Identify the parasite.
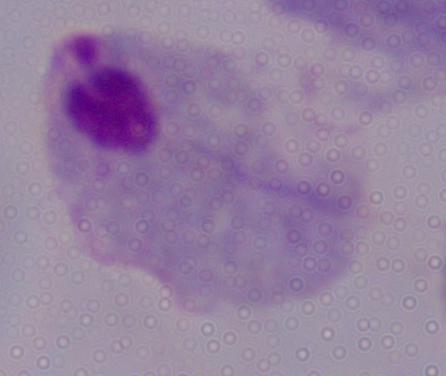
A trichomonad.

Summary:
  - Modality: micrograph
  - Magnification: 1000x